Evaluate for Plasmodium parasites.
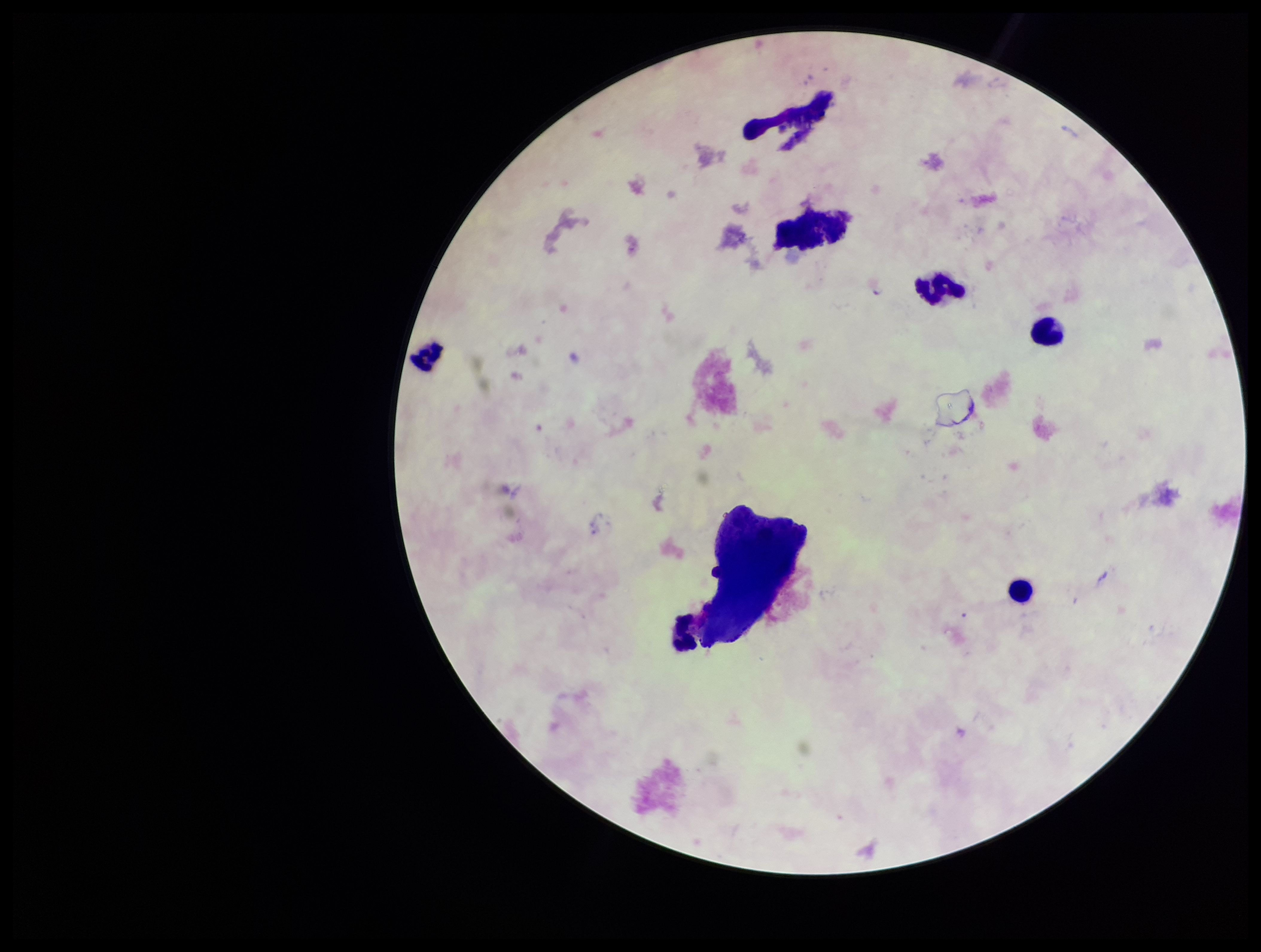

None identified.

Summary:
  - Patient malaria status: positive
  - Parasite count: 0
  - Stain: Giemsa
  - Capture: smartphone photograph through the microscope eyepiece
  - Image size: 1261×952 pixels
  - Field of view: one from this slide
  - Preparation: thick
  - Species reported for this patient: Plasmodium falciparum
  - Leukocyte count: 6